State which parasite is depicted.
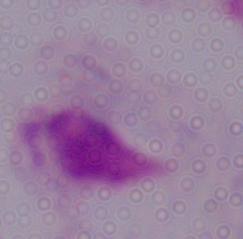

This is a trichomonad.

{
  "magnification": "1000x",
  "modality": "micrograph"
}